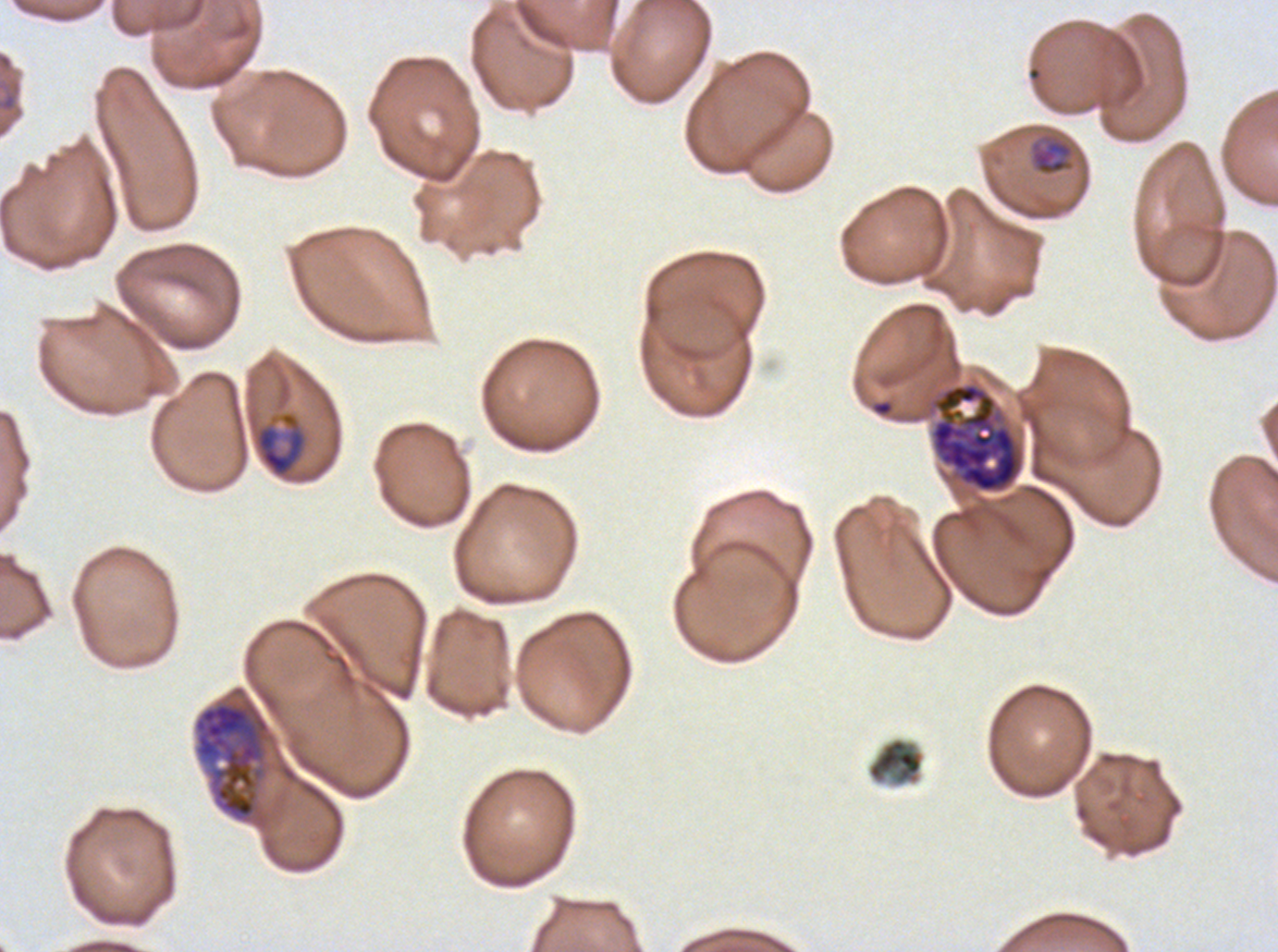
Approximate bounding boxes as (x1, y1, x2, y2) in pixels.
Summary:
  - Late-ring/early-trophozoite locations: (1029, 138, 1074, 176)
  - Debris locations: (866, 737, 926, 787)
  - Late schizont locations: (929, 382, 1026, 494)
  - Ring locations: (871, 399, 894, 417)
  - Mid trophozoite locations: (253, 410, 308, 480)
  - Early schizont locations: (192, 697, 272, 824)
  - Stain: Giemsa
  - Specimen: Plasmodium falciparum cultured ex vivo for 24 to 48 hours, from a patient in The Gambia
  - Preparation: thin blood film
  - Image size: 1278×952 pixels
  - Life-cycle stages observed: ring, late-ring/early-trophozoite, mid trophozoite, early schizont, late schizont
  - Field of view: one sub-image of a larger composite